Point out Plasmodium parasites and leukocytes.
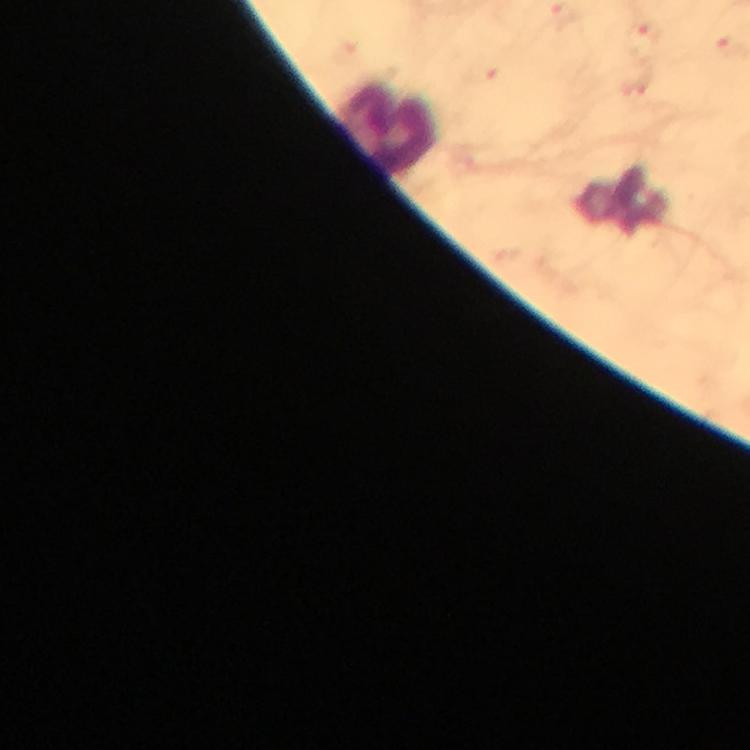

No Plasmodium parasites detected.
Approximate centers as [x, y] in pixels.
Leukocytes: [389, 128].

cropped from = a single field of view
preparation = thick blood film
capture = smartphone camera through the microscope
stain = Giemsa
context = from a malaria diagnostic workup
immersion oil = used
magnification = 100x
image size = 750×750 pixels